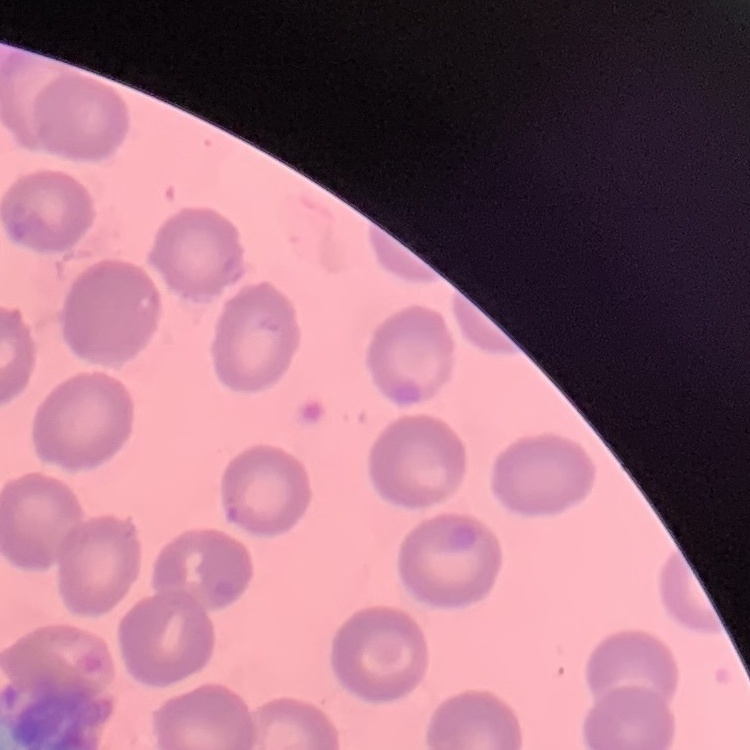

Summary:
  - Red blood cell morphology: no rouleaux formation
  - Image type: square crop of a larger photomicrograph
  - Stain: Field's or Giemsa
  - Preparation: thin blood film